Assess this cell for malaria.
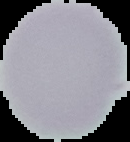
It is uninfected.

Summary:
  - Preparation: thin blood smear
  - Image type: segmented cell region with the area outside set to black
  - Image size: 130×142 pixels